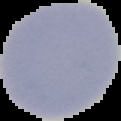

Cell region segmented out of the field of view; the surrounding area is masked to black. Result: negative for Plasmodium parasites. From a thin blood smear. Image is 121×121 pixels.